Point out each Plasmodium parasite.
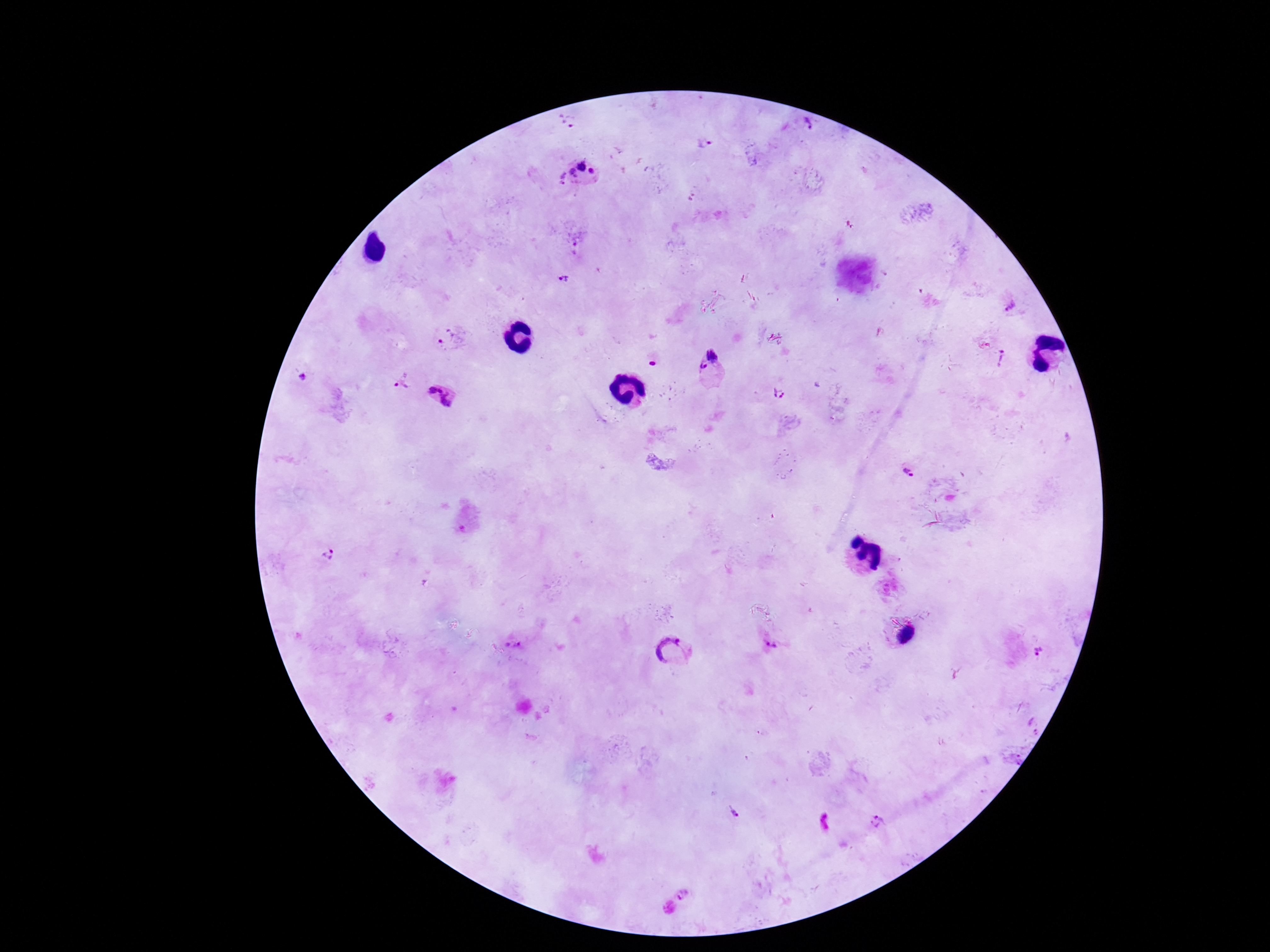
Approximate centers as [x, y] in pixels.
Plasmodium parasites: [568, 122], [807, 124], [707, 144], [578, 173], [576, 248], [564, 279], [1011, 307], [449, 337], [1003, 359], [711, 362], [652, 363], [300, 377], [402, 381], [779, 393], [441, 394], [908, 470], [328, 556], [768, 639], [512, 644], [674, 652], [1041, 654], [1033, 724], [1013, 758], [733, 813], [877, 822], [683, 894].

magnification = 100x
patient malaria status = infected
field of view = single
stain = Giemsa
image size = 1270×952 pixels
preparation = thick blood smear
capture = smartphone camera through the microscope eyepiece